Assess this cell for malaria.
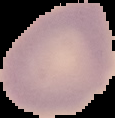

It is uninfected.

From a thin blood smear. Segmented cell region on a black background. Image is 115×118 pixels.